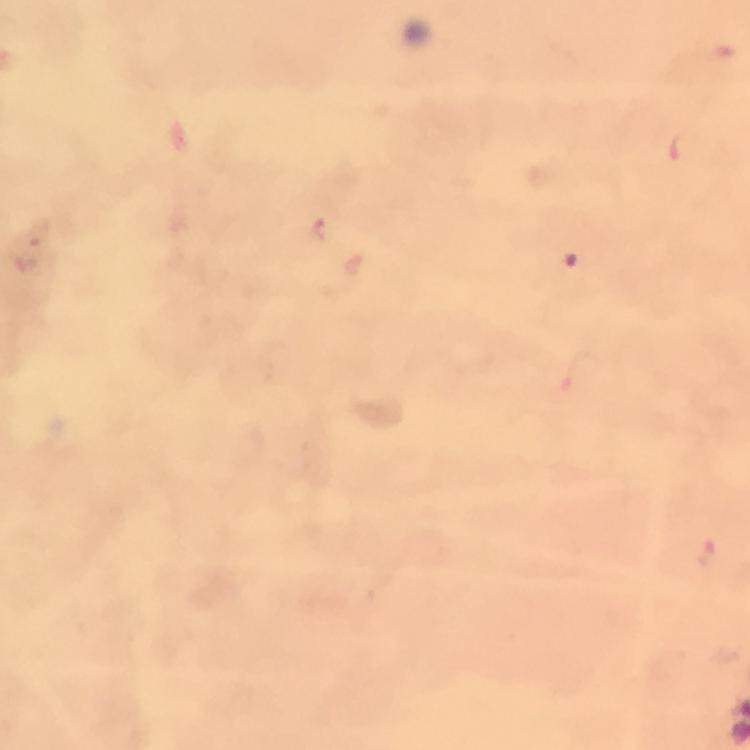

Approximate centers as {x, y} in pixels. Plasmodium parasite locations: {685, 148}, {320, 231}, {356, 265}, {580, 371}. From a malaria diagnostic workup. Giemsa stain. A crop from one field of view. Image is 750×750 pixels. Immersion oil applied. 100x magnification. Thick blood smear. Photographed with a smartphone mounted on the microscope.